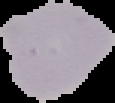
The area outside the segmented cell region is set to black. From a thin blood smear. Image is 115×103 pixels. Result: no malaria parasites detected.